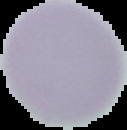
{
  "malaria_status": "uninfected",
  "image_size": "127×130 pixels",
  "preparation": "thin blood smear",
  "image_type": "cell region segmented out of the field of view; surrounding area masked to black"
}